Give the position of every malaria parasite.
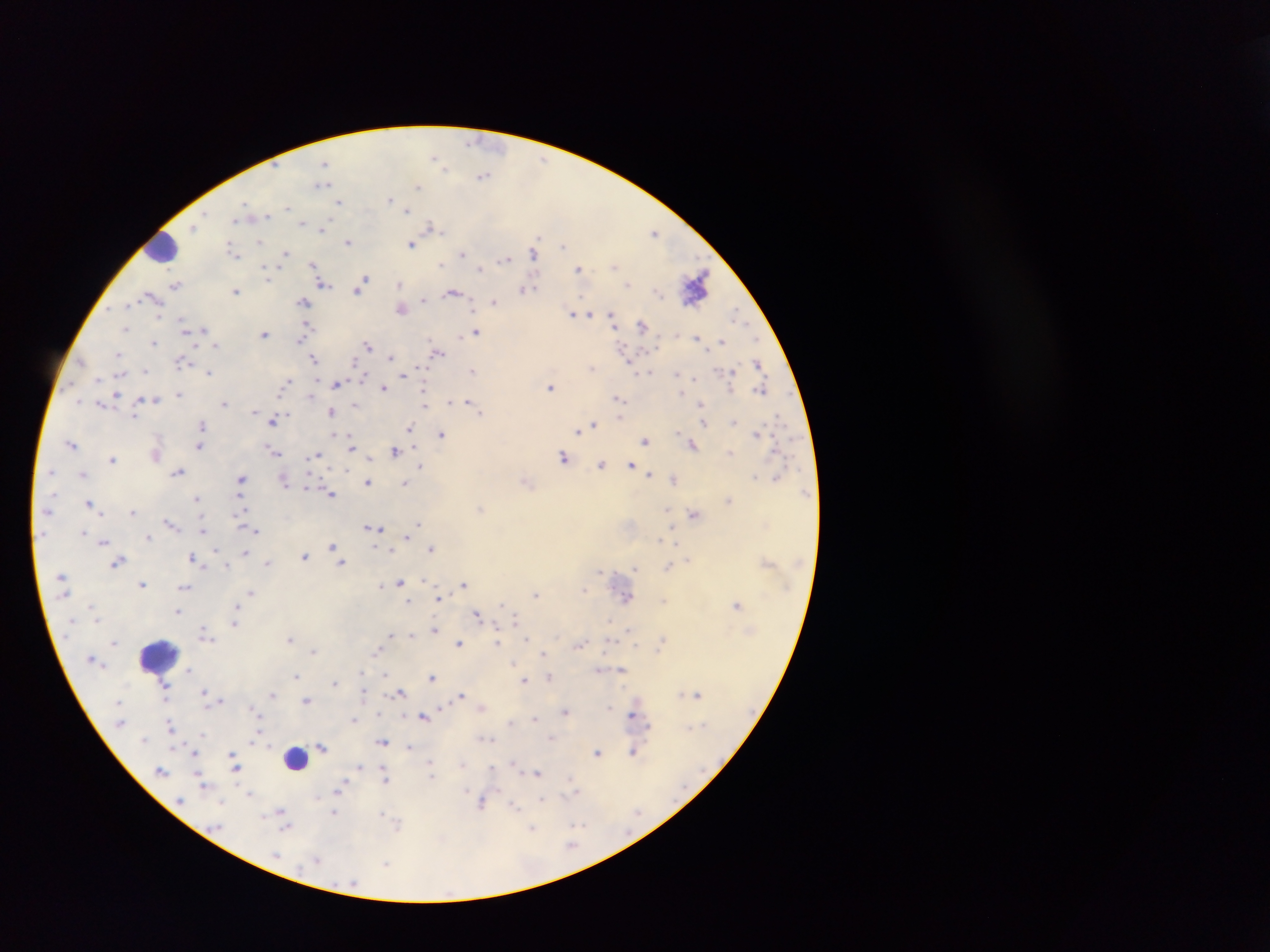
Approximate centers as x y in pixels.
Malaria parasites: 471 142; 434 158; 324 163; 443 166; 483 176; 322 184; 418 186; 390 200; 339 201; 245 205; 287 207; 408 209; 266 215; 236 220; 302 223; 431 226; 193 227; 323 228; 654 232; 261 241; 348 242; 411 244; 563 245; 233 252; 533 253; 285 254; 463 254; 504 258; 441 264; 313 265; 614 265; 481 269; 578 269; 318 272; 267 275; 697 281; 323 284; 399 284; 628 284; 175 285; 360 286; 526 289; 236 291; 452 293; 149 295; 423 299; 304 302; 495 302; 126 305; 402 308; 571 312; 591 313; 736 314; 611 317; 183 325; 642 325; 125 328; 204 329; 306 329; 476 331; 264 334; 697 338; 301 339; 756 339; 722 341; 154 343; 216 345; 368 345; 437 353; 118 354; 390 357; 313 359; 631 359; 182 362; 759 364; 592 368; 145 370; 472 370; 209 372; 650 373; 403 374; 678 374; 364 375; 694 377; 98 378; 336 384; 284 385; 384 387; 551 387; 424 388; 762 390; 114 395; 179 395; 311 396; 618 398; 155 399; 78 401; 449 401; 469 401; 700 403; 223 404; 356 404; 425 404; 254 410; 481 412; 331 413; 135 415; 620 416; 273 420; 735 421; 704 424; 594 425; 202 426; 411 429; 578 431; 757 433; 334 434; 442 435; 645 441; 71 444; 351 445; 692 445; 199 446; 272 451; 394 451; 730 453; 316 456; 562 458; 112 459; 601 465; 631 465; 421 466; 346 471; 179 472; 83 474; 649 474; 755 476; 776 477; 674 478; 241 480; 412 480; 284 483; 367 483; 405 483; 307 484; 331 493; 197 499; 728 500; 89 503; 480 508; 667 511; 133 512; 694 514; 169 523; 418 524; 374 528; 204 529; 256 530; 83 533; 148 537; 407 537; 659 539; 104 542; 676 543; 333 546; 431 548; 217 551; 245 553; 304 556; 191 558; 689 559; 118 562; 268 563; 341 563; 226 565; 635 567; 668 567; 600 572; 400 582; 463 583; 142 584; 380 586; 185 587; 585 589; 252 593; 536 594; 626 597; 438 599; 409 601; 737 604; 236 607; 178 611; 476 614; 516 619; 609 621; 234 622; 434 629; 629 630; 205 634; 391 635; 411 635; 290 637; 526 639; 497 641; 661 642; 458 643; 580 644; 313 651; 377 651; 542 653; 514 663; 189 670; 599 670; 622 670; 362 673; 385 675; 296 676; 431 677; 549 678; 524 680; 334 682; 205 692; 364 693; 401 693; 272 694; 460 694; 681 694; 698 695; 306 700; 221 701; 610 707; 253 709; 441 710; 565 712; 403 715; 424 716; 633 716; 535 718; 354 719; 509 723; 171 725; 202 734; 256 738; 550 738; 490 740; 382 742; 321 747; 409 747; 195 752; 633 752; 597 753; 234 761; 430 762; 514 764; 462 765; 360 766; 492 767; 236 768; 429 769; 161 771; 538 773; 431 775; 386 778; 201 783; 571 783; 341 785; 575 790; 466 791; 249 793; 317 796; 542 800; 180 801; 222 802; 483 803; 514 806; 335 809; 281 812; 334 813; 382 813; 265 814; 398 825; 576 825; 286 827; 532 828; 572 846; 276 855; 317 861; 386 864.

leukocyte locations = approximate centers as x y in pixels: 164 246; 157 655; 295 756
preparation = thick blood film
country = Ghana
image size = 1270×952 pixels
capture = mobile-phone photograph through a microscope
field of view = single